Evaluate for malaria.
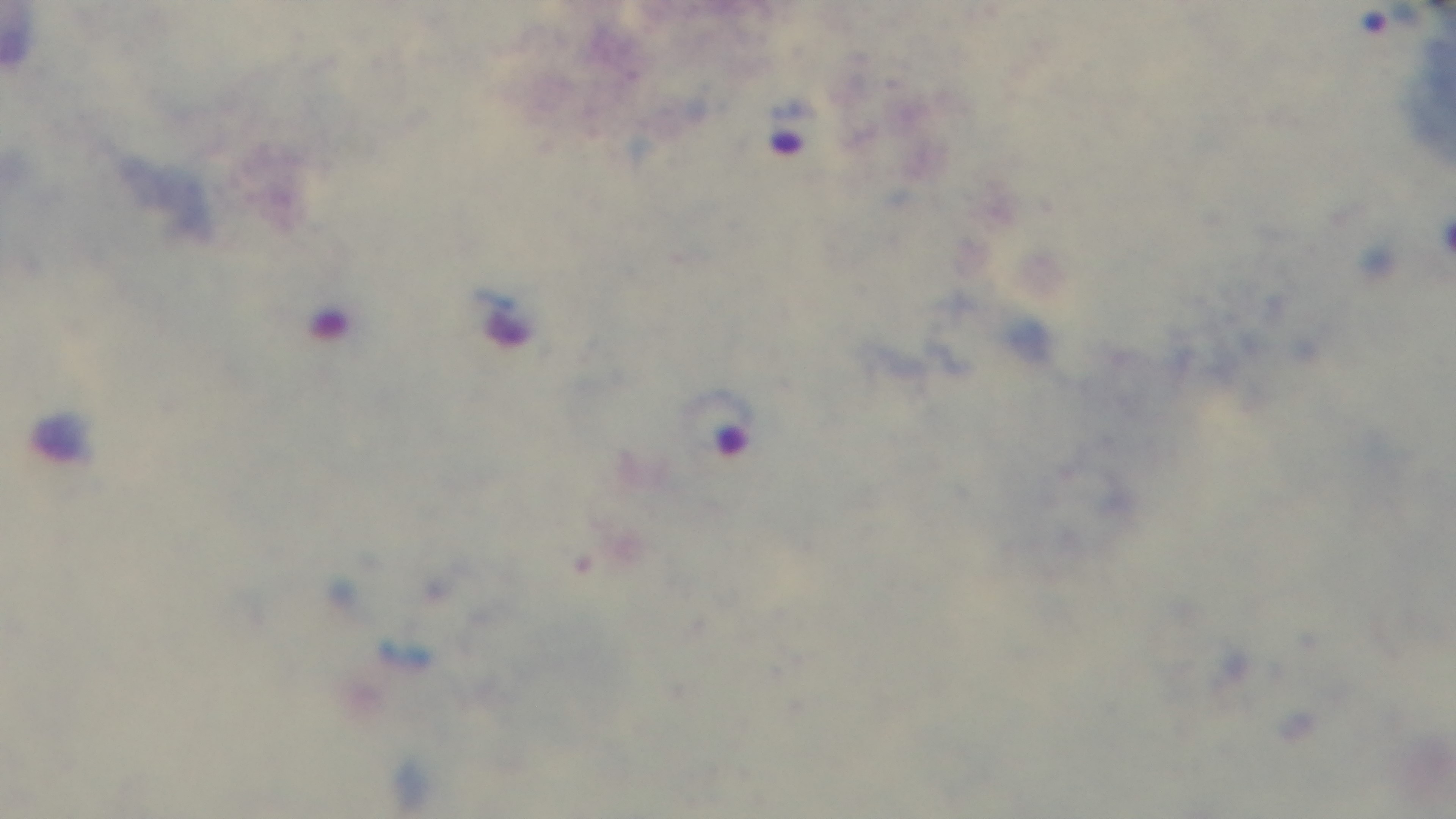
It is infected.

Summary:
  - Preparation: thick
  - Field of view: one from the slide
  - Objective: 100x oil immersion
  - Modality: light microscopy
  - Stain: Giemsa
  - Capture: mounted 4K digital camera